Comment on the morphology of the erythrocytes.
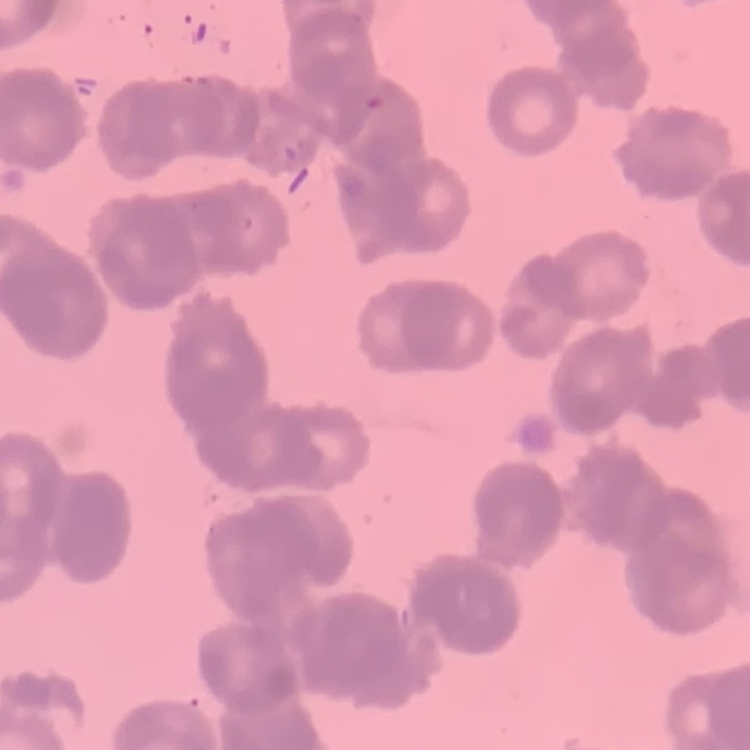

They show rouleaux formation.

Thin peripheral smear. Field's or Giemsa stain. Square crop of a larger photomicrograph.